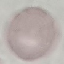

{
  "malaria_status": "uninfected",
  "image_type": "cell patch, automatically extracted from a larger field of view and resized to 64 × 64 pixels",
  "stain": "Giemsa",
  "capture": "smartphone through the microscope eyepiece",
  "preparation": "thin blood smear"
}